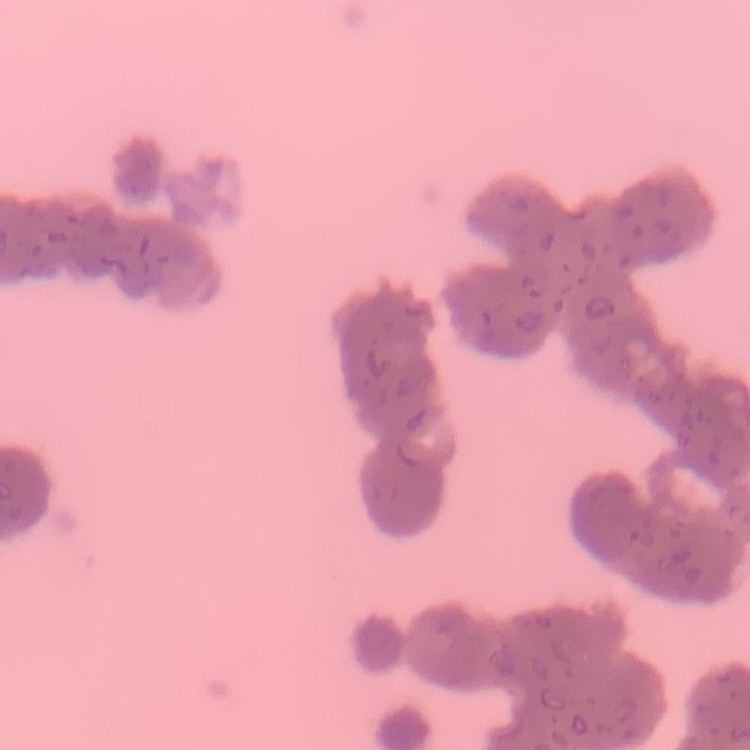
Summary:
  - Erythrocyte morphology: rouleaux formation
  - Stain: Field's or Giemsa
  - Preparation: thin blood smear
  - Image type: square crop of a larger photomicrograph